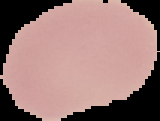
preparation = thin blood smear
image size = 160×121 pixels
image type = cell region segmented out of the field of view; surrounding area masked to black
result = no malaria parasites detected